Classify this cell by malaria status.
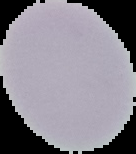

Uninfected.

Summary:
  - Image size: 136×154 pixels
  - Preparation: thin blood film
  - Image type: segmented cell region on a black background